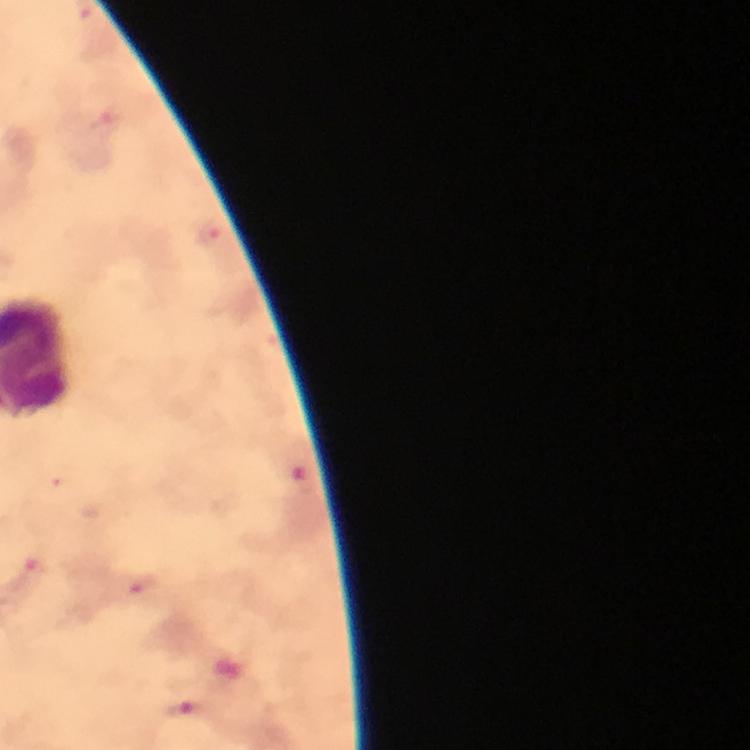

{
  "stain": "Giemsa",
  "immersion_oil": "applied",
  "plasmodium_parasite_locations": "approximate centers as (x, y) in pixels: (211, 234), (32, 572), (144, 585), (186, 710)",
  "context": "from a diagnostic examination for malaria",
  "capture": "smartphone mounted on the microscope",
  "image_size": "750×750 pixels",
  "magnification": "100x",
  "preparation": "thick smear",
  "cropped_from": "a single field of view"
}